Name the cell type shown.
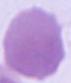

This is an erythrocyte.

1000x magnification. Photomicrograph.